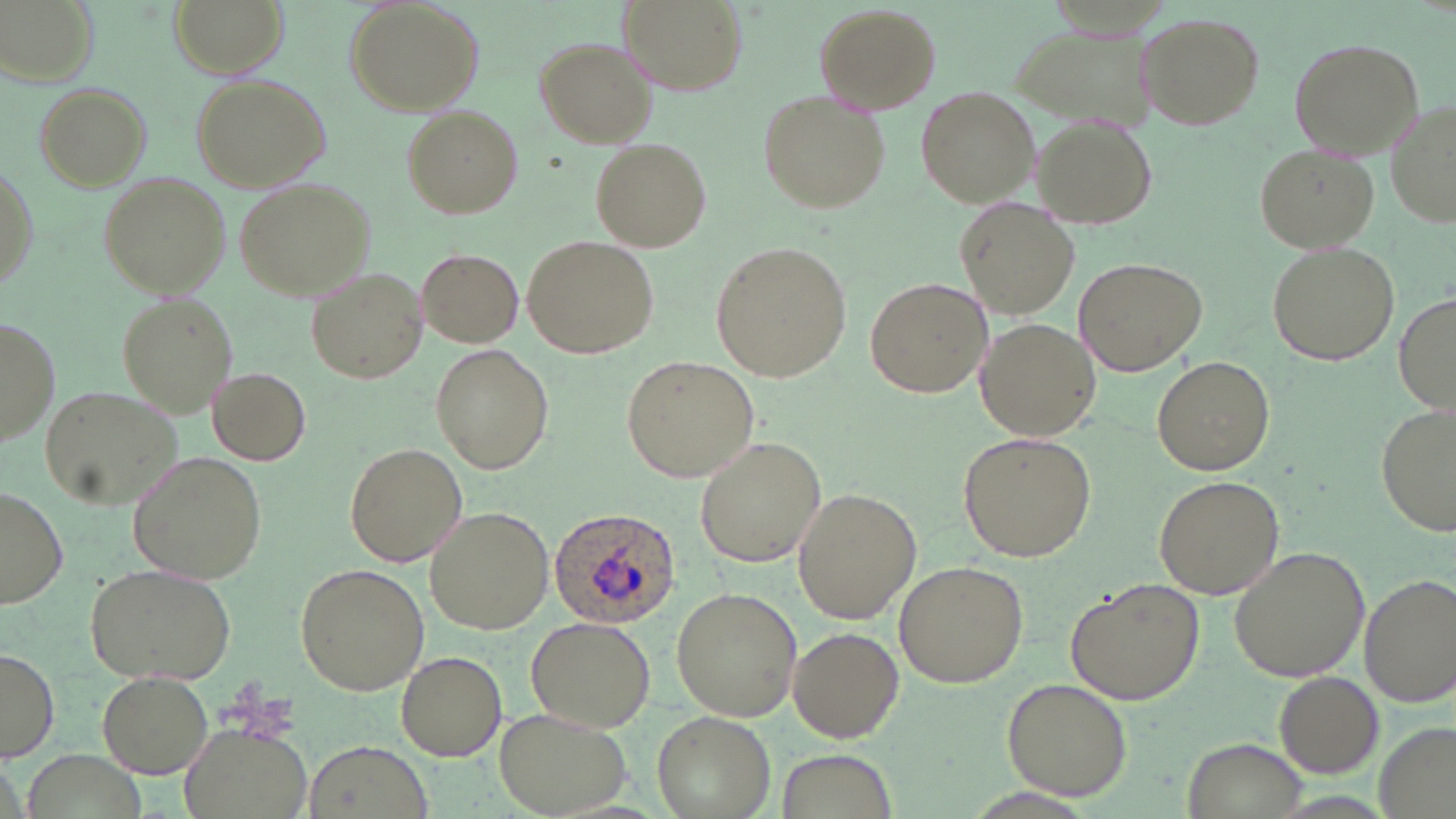

Plasmodium ovale-infected red blood cell locations = approximate bounding boxes as named x1/y1/x2/y2 corners in pixels: (x1=549, y1=507, x2=680, y2=628)
slide-level diagnosis = Plasmodium ovale
preparation = thin blood film
field of view = one of a larger specimen
stain = May-Grünwald-Giemsa
uninfected red blood cell locations = approximate bounding boxes as named x1/y1/x2/y2 corners in pixels: (x1=3, y1=0, x2=98, y2=87), (x1=170, y1=0, x2=284, y2=76), (x1=618, y1=0, x2=746, y2=94), (x1=343, y1=1, x2=485, y2=115), (x1=813, y1=3, x2=939, y2=113), (x1=1135, y1=12, x2=1264, y2=131), (x1=1009, y1=26, x2=1161, y2=135), (x1=533, y1=36, x2=659, y2=148), (x1=1287, y1=37, x2=1424, y2=158), (x1=191, y1=72, x2=334, y2=194), (x1=33, y1=80, x2=151, y2=190), (x1=915, y1=87, x2=1038, y2=207), (x1=759, y1=91, x2=889, y2=212), (x1=1385, y1=100, x2=1456, y2=230), (x1=402, y1=105, x2=524, y2=219), (x1=1032, y1=116, x2=1159, y2=229), (x1=592, y1=138, x2=710, y2=251), (x1=1253, y1=143, x2=1380, y2=254), (x1=1, y1=159, x2=38, y2=303), (x1=98, y1=171, x2=231, y2=297), (x1=233, y1=176, x2=376, y2=301), (x1=955, y1=198, x2=1079, y2=319), (x1=522, y1=235, x2=660, y2=359), (x1=1266, y1=240, x2=1399, y2=367), (x1=709, y1=241, x2=852, y2=380), (x1=415, y1=250, x2=524, y2=346), (x1=1075, y1=256, x2=1207, y2=375), (x1=305, y1=266, x2=428, y2=387), (x1=865, y1=276, x2=992, y2=398), (x1=1394, y1=289, x2=1455, y2=415), (x1=115, y1=293, x2=236, y2=418), (x1=1, y1=318, x2=59, y2=446), (x1=977, y1=319, x2=1101, y2=440), (x1=432, y1=345, x2=552, y2=473), (x1=621, y1=353, x2=760, y2=480), (x1=1152, y1=356, x2=1274, y2=477), (x1=207, y1=367, x2=311, y2=465), (x1=37, y1=384, x2=183, y2=509), (x1=1376, y1=406, x2=1455, y2=538), (x1=959, y1=429, x2=1099, y2=561), (x1=693, y1=435, x2=826, y2=568), (x1=345, y1=442, x2=467, y2=568), (x1=130, y1=452, x2=266, y2=582), (x1=1151, y1=476, x2=1284, y2=600), (x1=792, y1=488, x2=920, y2=623), (x1=0, y1=489, x2=68, y2=608), (x1=424, y1=508, x2=550, y2=635), (x1=1229, y1=546, x2=1372, y2=682), (x1=893, y1=560, x2=1029, y2=688), (x1=84, y1=562, x2=236, y2=685), (x1=294, y1=562, x2=429, y2=695), (x1=1359, y1=575, x2=1455, y2=705), (x1=1065, y1=578, x2=1206, y2=704), (x1=670, y1=587, x2=803, y2=722), (x1=525, y1=613, x2=657, y2=733), (x1=788, y1=625, x2=904, y2=744), (x1=0, y1=647, x2=58, y2=762), (x1=396, y1=650, x2=506, y2=760), (x1=1272, y1=671, x2=1384, y2=778), (x1=98, y1=672, x2=213, y2=778), (x1=1001, y1=677, x2=1135, y2=801), (x1=651, y1=707, x2=776, y2=817), (x1=496, y1=709, x2=632, y2=817), (x1=175, y1=718, x2=316, y2=819), (x1=1185, y1=737, x2=1309, y2=819), (x1=302, y1=740, x2=434, y2=819), (x1=770, y1=747, x2=900, y2=819), (x1=27, y1=749, x2=139, y2=819)
image size = 1456×819 pixels
modality = light microscopy
magnification = 1000x